Give the position of every leukocyte visible.
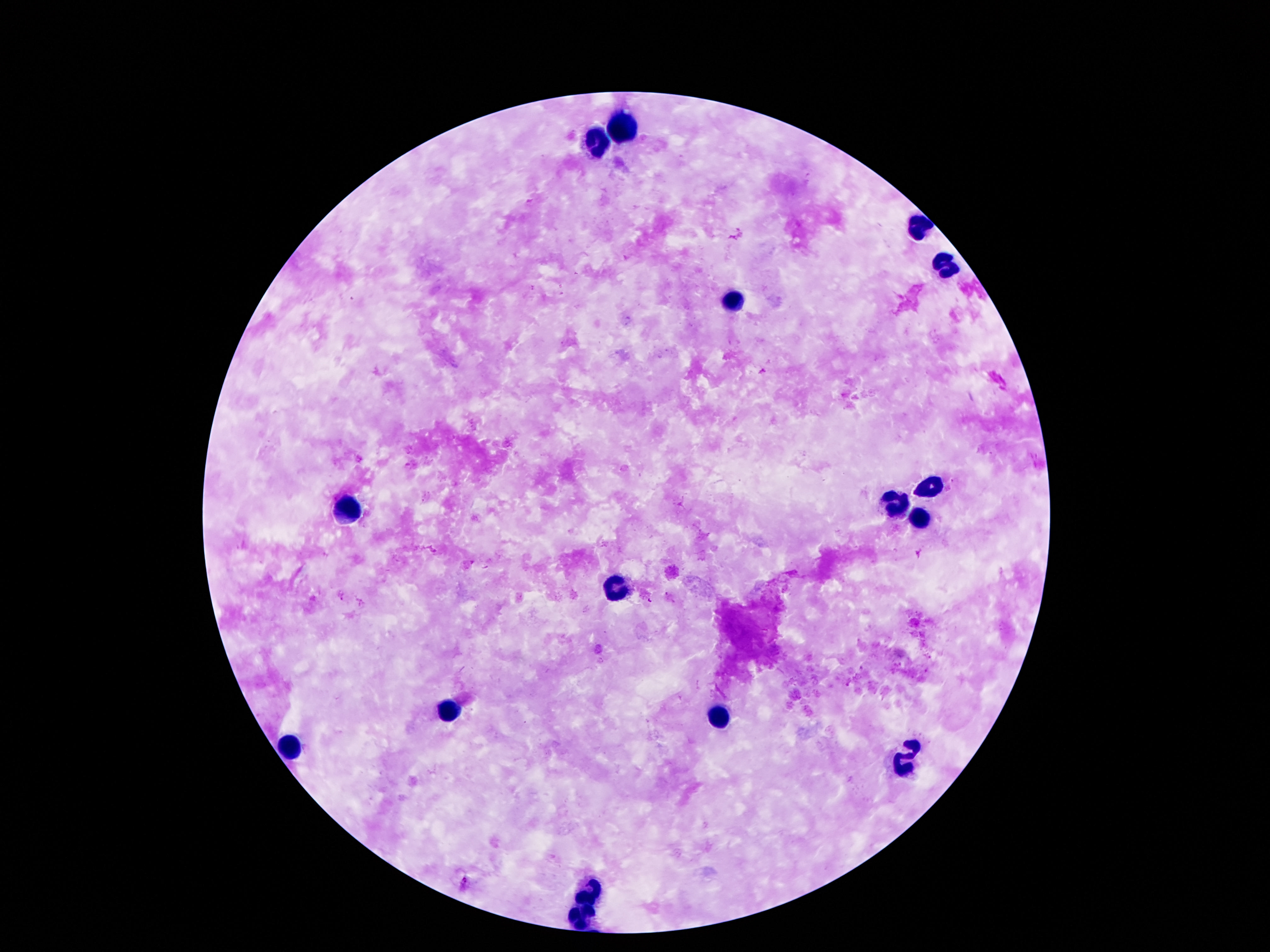

Approximate centers as [x, y] in pixels.
Leukocytes: [626, 128], [600, 143], [917, 227], [948, 264], [731, 302], [929, 486], [896, 502], [341, 511], [917, 520], [619, 589], [448, 708], [717, 715], [292, 748], [906, 759], [591, 892], [581, 914].

stain = Giemsa
preparation = thick peripheral-blood smear
magnification = 100x
patient malaria status = negative
image size = 1270×952 pixels
capture = smartphone camera through the microscope eyepiece
field of view = one from this slide